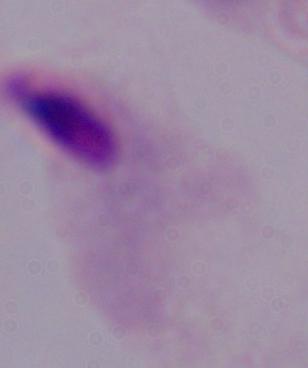

Summary:
  - Modality: micrograph
  - Identification: trichomonad
  - Magnification: 1000x